Give the extent of all Plasmodium falciparum-infected red blood cells.
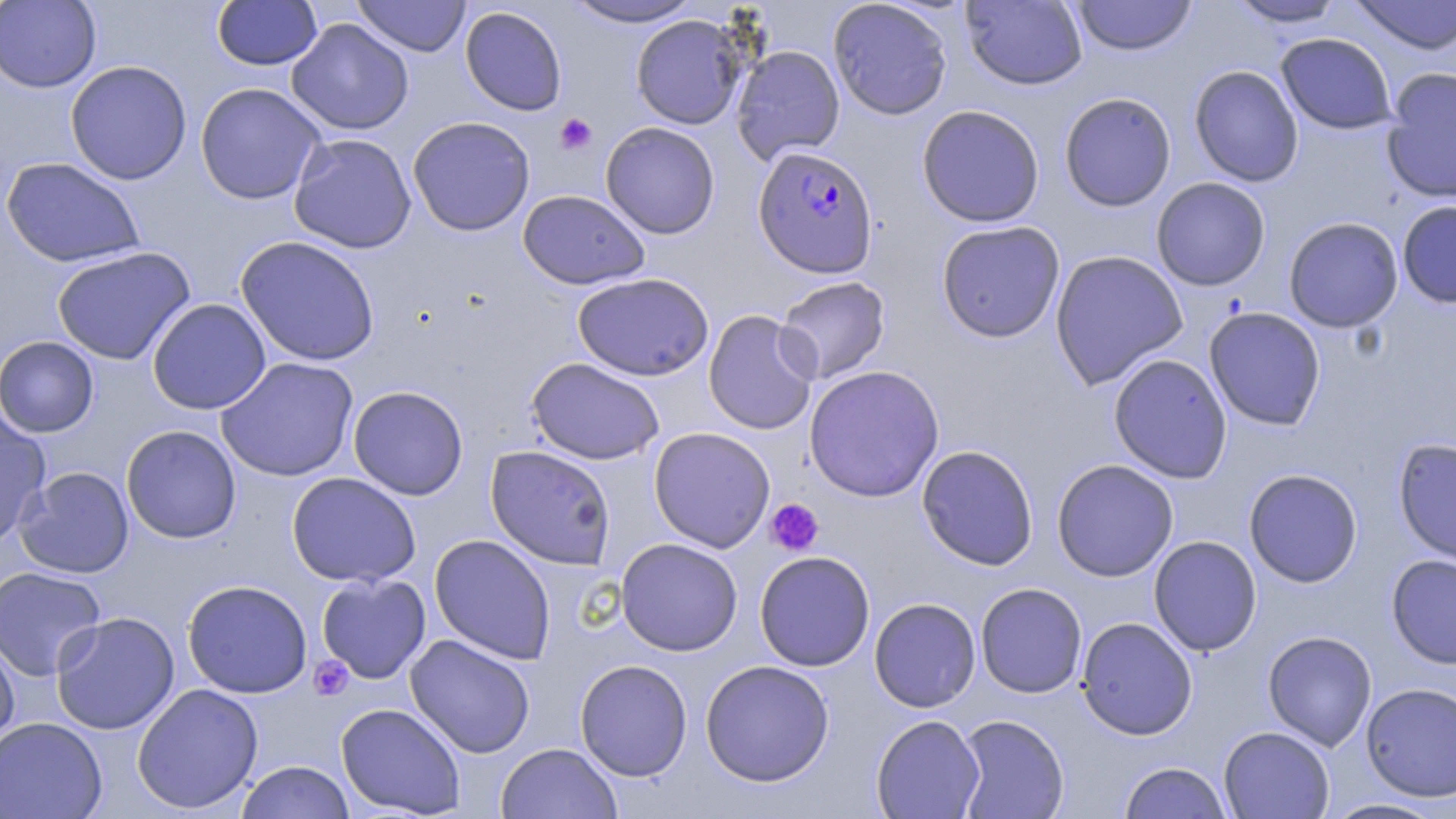

Approximate bounding boxes as named x1/y1/x2/y2 corners in pixels.
Plasmodium falciparum-infected red blood cells: (x1=752, y1=146, x2=879, y2=279).

slide_level_diagnosis: Plasmodium falciparum
image_size: 1456×819 pixels
field_of_view: one of a larger specimen
stain: May-Grünwald-Giemsa
uninfected_red_blood_cell_locations: 'approximate bounding boxes as named x1/y1/x2/y2 corners in pixels: (x1=0, y1=0, x2=101, y2=93), (x1=212, y1=0, x2=322, y2=71), (x1=353, y1=0, x2=471, y2=57), (x1=562, y1=0, x2=705, y2=28), (x1=828, y1=0, x2=953, y2=120), (x1=961, y1=0, x2=1088, y2=90), (x1=1070, y1=0, x2=1198, y2=56), (x1=1226, y1=0, x2=1349, y2=28), (x1=1348, y1=0, x2=1456, y2=55), (x1=459, y1=6, x2=567, y2=116), (x1=630, y1=14, x2=747, y2=130), (x1=286, y1=18, x2=414, y2=136), (x1=1275, y1=32, x2=1398, y2=135), (x1=731, y1=45, x2=845, y2=164), (x1=65, y1=60, x2=192, y2=185), (x1=1188, y1=65, x2=1304, y2=187), (x1=1381, y1=68, x2=1456, y2=203), (x1=195, y1=82, x2=326, y2=205), (x1=1059, y1=91, x2=1177, y2=212), (x1=916, y1=104, x2=1045, y2=228), (x1=408, y1=116, x2=535, y2=236), (x1=600, y1=121, x2=720, y2=239), (x1=288, y1=133, x2=417, y2=254), (x1=1, y1=157, x2=145, y2=268), (x1=1151, y1=177, x2=1270, y2=291), (x1=517, y1=190, x2=650, y2=290), (x1=1397, y1=200, x2=1456, y2=308), (x1=1283, y1=217, x2=1403, y2=333), (x1=935, y1=220, x2=1065, y2=343), (x1=236, y1=235, x2=380, y2=366), (x1=51, y1=246, x2=196, y2=364), (x1=1049, y1=249, x2=1188, y2=389), (x1=572, y1=272, x2=714, y2=381), (x1=775, y1=276, x2=890, y2=384), (x1=147, y1=298, x2=271, y2=414), (x1=1204, y1=306, x2=1326, y2=431), (x1=703, y1=309, x2=819, y2=435), (x1=0, y1=336, x2=99, y2=437), (x1=1108, y1=353, x2=1232, y2=483), (x1=216, y1=356, x2=359, y2=482), (x1=526, y1=357, x2=665, y2=465), (x1=803, y1=364, x2=944, y2=502), (x1=348, y1=385, x2=469, y2=500), (x1=0, y1=407, x2=52, y2=547), (x1=121, y1=424, x2=241, y2=543), (x1=648, y1=427, x2=776, y2=553), (x1=1393, y1=437, x2=1456, y2=568), (x1=916, y1=444, x2=1038, y2=570), (x1=485, y1=445, x2=616, y2=569), (x1=1051, y1=459, x2=1179, y2=581), (x1=15, y1=466, x2=134, y2=578), (x1=1243, y1=468, x2=1363, y2=588), (x1=286, y1=472, x2=421, y2=587), (x1=429, y1=534, x2=556, y2=664), (x1=1148, y1=535, x2=1262, y2=656), (x1=615, y1=538, x2=743, y2=656), (x1=754, y1=551, x2=875, y2=671), (x1=1386, y1=553, x2=1456, y2=669), (x1=0, y1=566, x2=106, y2=681), (x1=316, y1=573, x2=431, y2=684), (x1=182, y1=579, x2=313, y2=698), (x1=975, y1=582, x2=1087, y2=698), (x1=869, y1=597, x2=981, y2=712), (x1=51, y1=611, x2=180, y2=735), (x1=1076, y1=617, x2=1198, y2=740), (x1=1262, y1=630, x2=1377, y2=752), (x1=0, y1=633, x2=21, y2=752), (x1=405, y1=634, x2=535, y2=758), (x1=574, y1=659, x2=693, y2=782), (x1=700, y1=659, x2=835, y2=787), (x1=1361, y1=682, x2=1456, y2=802), (x1=131, y1=683, x2=264, y2=814), (x1=335, y1=702, x2=466, y2=817), (x1=871, y1=714, x2=985, y2=818), (x1=954, y1=714, x2=1069, y2=818), (x1=0, y1=717, x2=107, y2=819), (x1=1219, y1=726, x2=1335, y2=818), (x1=496, y1=742, x2=621, y2=819), (x1=236, y1=760, x2=356, y2=819), (x1=1118, y1=762, x2=1233, y2=818), (x1=1320, y1=798, x2=1453, y2=819)'
preparation: thin blood smear
platelet_locations: 'approximate bounding boxes as named x1/y1/x2/y2 corners in pixels: (x1=555, y1=113, x2=597, y2=155), (x1=765, y1=499, x2=824, y2=556), (x1=309, y1=656, x2=354, y2=700)'
modality: light microscopy
magnification: 1000x